Identify the parasite.
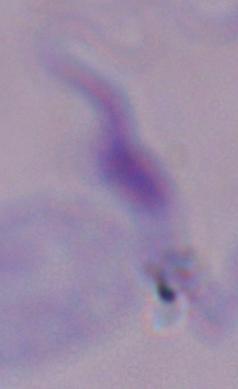

A trypanosome.

modality = micrograph
magnification = 1000x